Assess this cell for malaria.
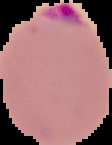

Parasitized.

Summary:
  - Image size: 112×145 pixels
  - Preparation: thin blood film
  - Image type: segmented cell region on a black background